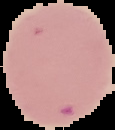

Summary:
  - Image type: segmented cell region on a black background
  - Image size: 115×130 pixels
  - Result: malaria parasites identified
  - Preparation: thin blood smear